Classify this cell by malaria status.
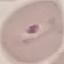

It is parasitized.

Thin smear of blood. Cell patch, automatically extracted from a larger field of view and resized to 64 × 64 pixels. Acquired by smartphone through the microscope eyepiece. Giemsa-stained preparation.